Describe the morphology of the erythrocytes.
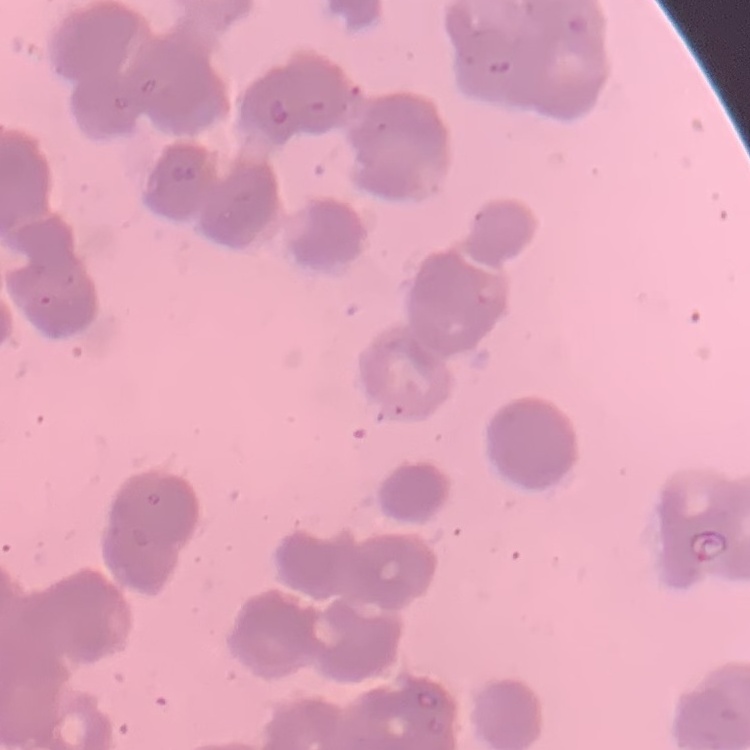
They show rouleaux formation.

image_type: square crop of a larger photomicrograph
stain: Field's or Giemsa
preparation: thin blood film